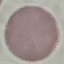

Summary:
  - Result: no malaria parasites detected
  - Image type: cell patch, automatically extracted from a larger field of view and resized to 64 × 64 pixels
  - Stain: Giemsa
  - Capture: smartphone camera at the microscope eyepiece
  - Preparation: thin blood film